Name the blood parasite species.
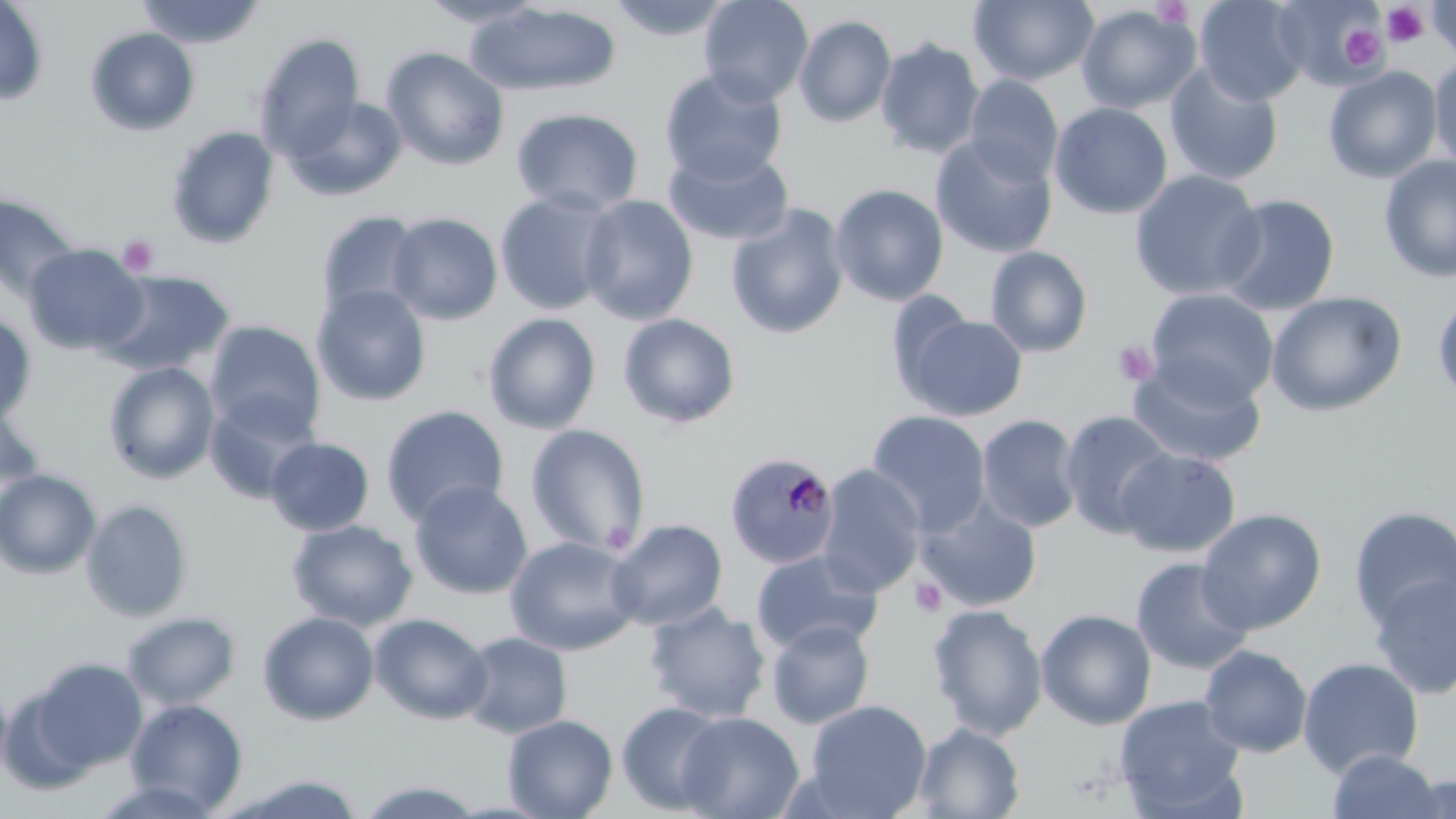
Plasmodium malariae.

Approximate bounding boxes as (x1,y1)-(x2,y2) corner pairs in pixels. Uninfected red blood cell locations: (135,0)-(265,49), (417,0)-(547,28), (605,0)-(736,41), (698,0)-(814,106), (968,0)-(1099,86), (1194,0)-(1309,105), (0,1)-(49,106), (1272,1)-(1387,90), (1427,1)-(1456,61), (466,3)-(621,96), (1076,5)-(1201,113), (793,14)-(897,127), (84,27)-(200,136), (254,32)-(367,155), (875,37)-(985,159), (381,46)-(510,171), (1429,56)-(1456,172), (1164,62)-(1284,186), (1323,65)-(1443,184), (659,68)-(788,185), (963,75)-(1063,185), (283,94)-(408,202), (1049,102)-(1173,219), (511,107)-(644,216), (166,125)-(280,249), (930,134)-(1058,259), (663,145)-(794,246), (1378,154)-(1456,284), (1129,169)-(1266,301), (829,183)-(949,306), (494,191)-(618,315), (1214,193)-(1341,316), (0,194)-(79,304), (577,194)-(699,326), (726,204)-(850,340), (316,210)-(425,321), (387,212)-(503,325), (23,243)-(147,357), (985,245)-(1094,357), (96,269)-(234,377), (312,285)-(432,407), (1145,289)-(1279,406), (1265,291)-(1407,417), (1432,292)-(1456,408), (899,312)-(1028,420), (482,313)-(602,434), (616,313)-(741,428), (0,314)-(37,425), (204,321)-(327,440), (1127,358)-(1267,469), (102,362)-(220,484), (203,394)-(318,504), (0,403)-(46,510), (380,405)-(509,526), (866,409)-(991,536), (1059,410)-(1177,539), (976,414)-(1083,534), (525,424)-(651,557), (265,437)-(375,536), (1116,447)-(1241,558), (815,464)-(927,598), (0,468)-(101,578), (408,479)-(533,599), (916,497)-(1043,612), (80,499)-(193,622), (1348,506)-(1456,630), (1196,508)-(1327,635), (606,518)-(728,630), (286,519)-(418,631), (504,536)-(642,655), (750,549)-(883,656), (1130,556)-(1256,675), (1368,571)-(1456,699), (643,601)-(772,722), (927,603)-(1048,740), (1035,608)-(1157,730), (121,611)-(242,710), (257,611)-(380,725), (368,612)-(493,724), (766,619)-(875,729), (458,631)-(573,739), (1199,644)-(1313,757), (30,657)-(148,771), (1298,657)-(1424,778), (0,676)-(13,787), (1114,694)-(1247,817), (125,699)-(248,813), (803,699)-(933,819), (616,701)-(728,814), (676,711)-(804,819), (503,714)-(618,818), (913,723)-(1025,818), (1327,749)-(1445,819), (220,773)-(369,818), (1395,773)-(1456,819), (352,779)-(489,818). Plasmodium malariae-infected red blood cell locations: (724,451)-(842,569). Platelet locations: (1149,0)-(1193,28), (1381,3)-(1430,48), (1340,23)-(1388,70), (117,235)-(160,277), (1113,340)-(1158,386), (909,577)-(947,618). Light microscopy. 1000x magnification. May-Grünwald-Giemsa stain. Image is 1456×819 pixels. Thin blood smear. Single field of view.